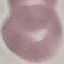

Result: negative for malaria parasites. Photographed with a smartphone camera at the microscope eyepiece. Thin smear of blood. Automatically extracted cell patch, resized to 64 × 64 pixels. Giemsa stain.